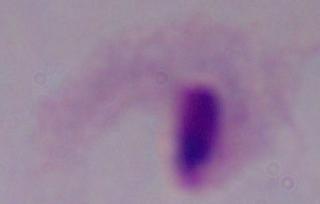

magnification = 1000x
modality = micrograph
identification = trichomonad